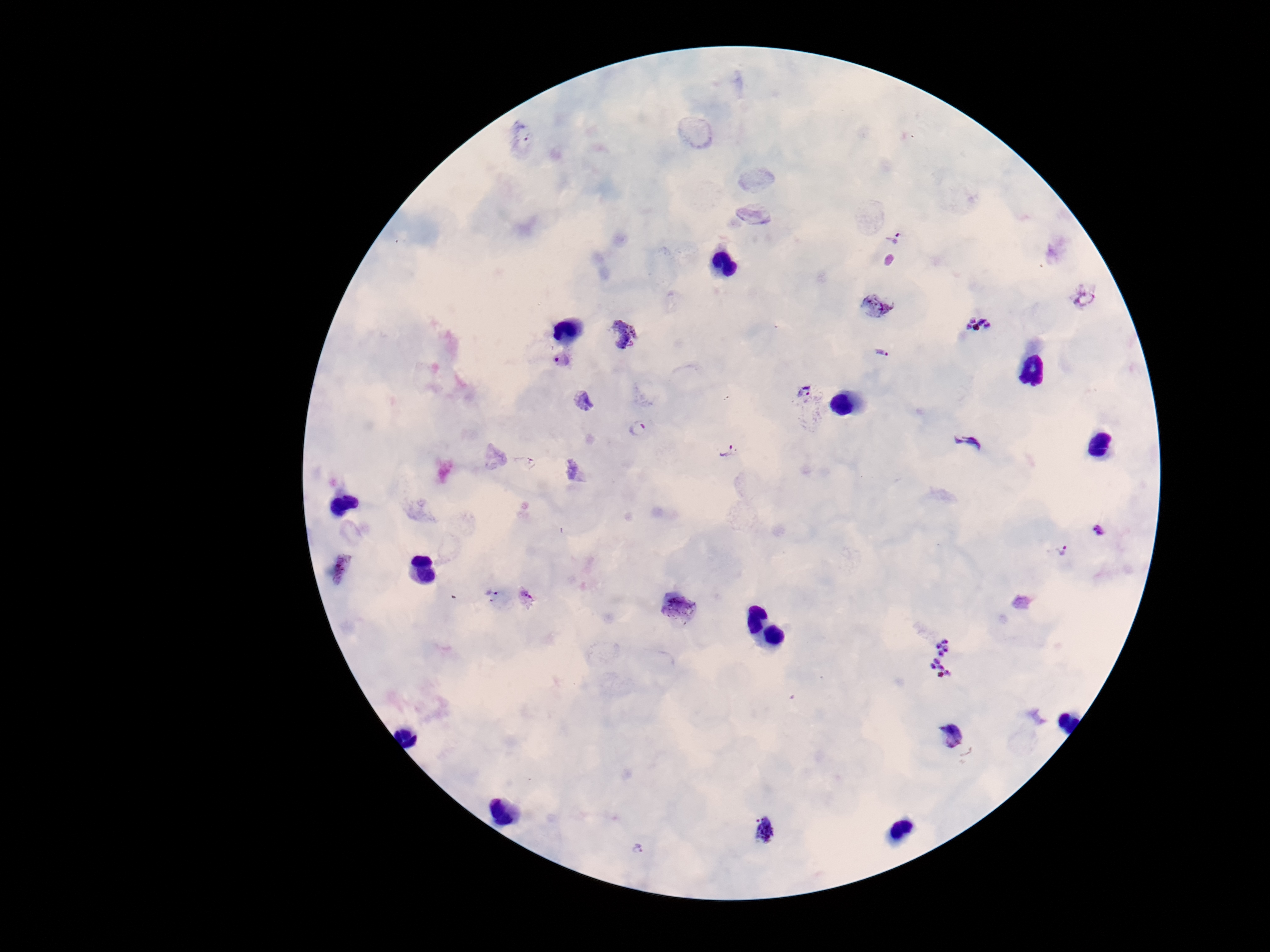

Approximate object centers, in pixels from the top-left corner. Plasmodium parasite locations: (x=894, y=238), (x=1087, y=297), (x=877, y=305), (x=978, y=324), (x=620, y=334), (x=883, y=354), (x=563, y=358), (x=807, y=398), (x=637, y=428), (x=969, y=444), (x=728, y=450), (x=1101, y=530), (x=1061, y=549), (x=343, y=569), (x=491, y=592), (x=526, y=597), (x=678, y=608), (x=947, y=658), (x=956, y=738), (x=765, y=830), (x=639, y=849). Patient malaria status: infected. One field from this slide. Image is 1270×952 pixels. 100x magnification. Photographed through the microscope eyepiece with a smartphone camera. Giemsa stain. Thick peripheral-blood smear.